Comment on the morphology of the erythrocytes.
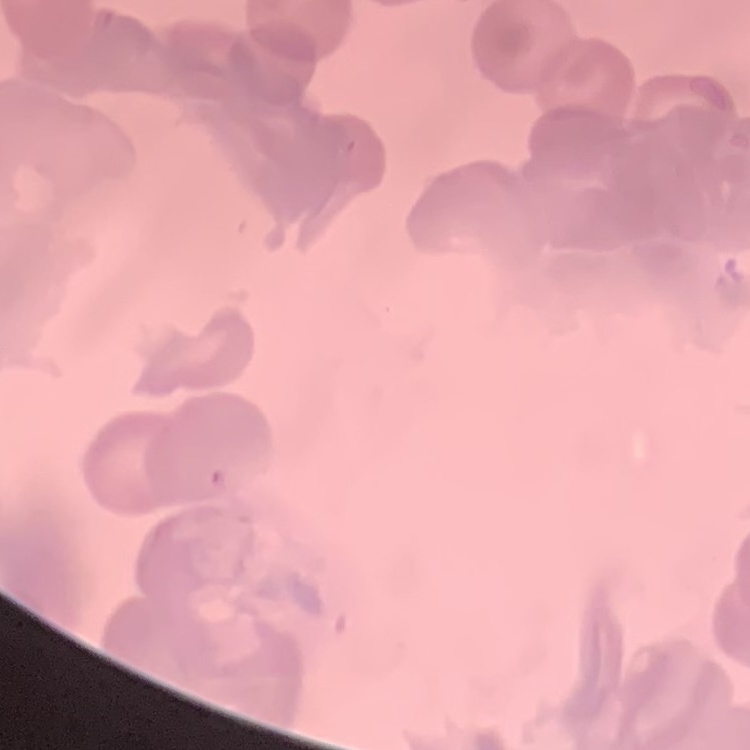
They show no rouleaux formation.

One tile cut from a larger photomicrograph. Thin peripheral smear. Field's or Giemsa stain.